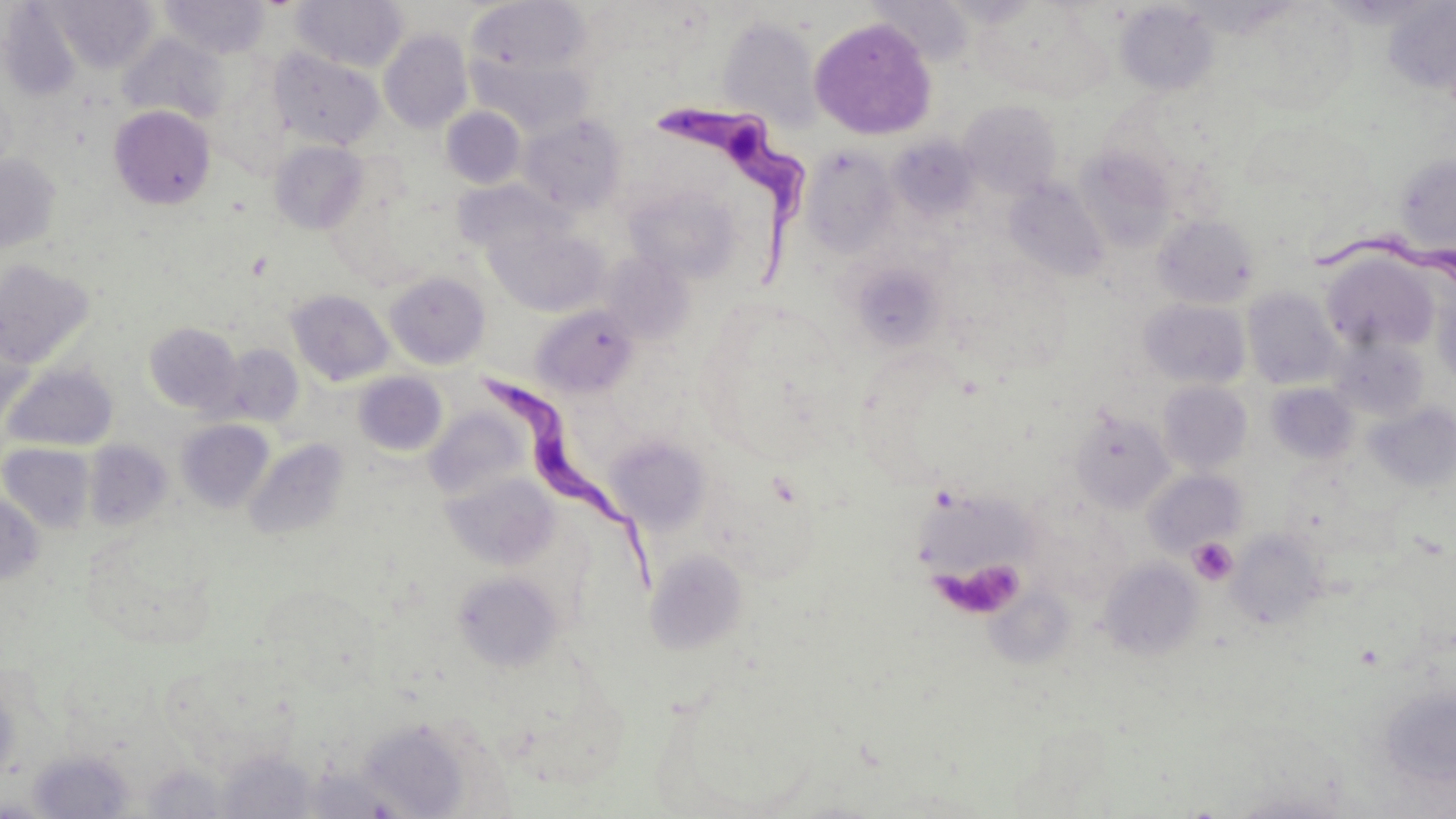

Summary:
  - Coordinate format: approximate bounding boxes as (x1,y1)-(x2,y2) corner pairs in pixels
  - Trypanosoma brucei locations: (660,102)-(812,292), (1306,236)-(1453,285), (489,373)-(672,596)
  - Uninfected red blood cell locations: (160,0)-(271,58), (292,0)-(407,71), (868,0)-(975,65), (48,1)-(161,74), (467,2)-(591,80), (1115,2)-(1218,96), (1383,3)-(1456,94), (979,4)-(1111,99), (1241,5)-(1359,113), (718,17)-(823,131), (809,18)-(940,141), (379,29)-(473,133), (119,32)-(230,124), (269,48)-(385,151), (471,54)-(594,138), (959,100)-(1063,198), (109,105)-(215,209), (441,107)-(526,189), (519,113)-(626,215), (889,136)-(979,222), (269,140)-(368,234), (802,146)-(899,259), (1075,148)-(1176,251), (1395,153)-(1456,254), (0,154)-(60,252), (1005,180)-(1109,282), (458,183)-(561,258), (626,185)-(740,283), (1153,214)-(1259,308), (486,224)-(608,316), (600,251)-(693,344), (1322,254)-(1436,352), (0,259)-(96,370), (852,264)-(945,350), (384,271)-(490,369), (1242,288)-(1342,389), (286,289)-(394,386), (1433,290)-(1456,386), (1139,299)-(1250,389), (531,304)-(638,398), (0,321)-(36,428), (145,322)-(241,414), (1330,336)-(1428,420), (219,343)-(304,426), (3,364)-(118,452), (353,372)-(448,456), (1157,381)-(1252,475), (1266,383)-(1359,464), (1364,402)-(1456,494), (425,407)-(531,501), (1069,409)-(1176,513), (176,419)-(275,514), (606,434)-(712,534), (244,438)-(349,541), (84,440)-(172,532), (1,443)-(95,533), (1143,469)-(1246,556), (442,471)-(559,570), (0,492)-(43,587), (81,527)-(218,651), (1227,529)-(1328,629), (644,548)-(749,655), (1099,557)-(1204,659), (452,571)-(563,671), (26,749)-(136,817), (140,763)-(230,818), (304,767)-(401,818), (1225,788)-(1351,818)
  - Platelet locations: (1188,537)-(1238,585), (941,562)-(1026,618)
  - Slide-level diagnosis: Trypanosoma brucei
  - Modality: light microscopy
  - Preparation: thin blood smear
  - Field of view: single
  - Image size: 1456×819 pixels
  - Magnification: 1000x
  - Stain: May-Grünwald-Giemsa